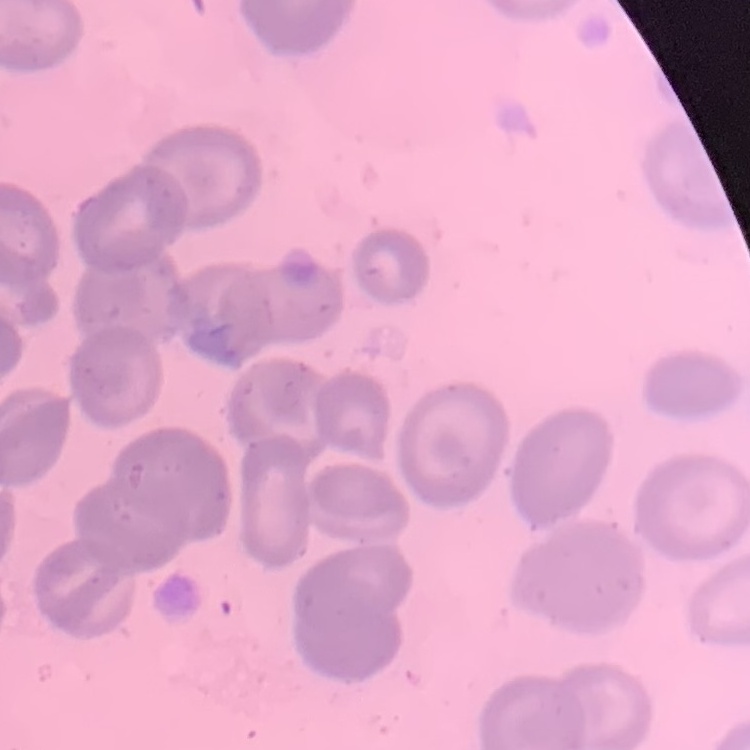
Summary:
  - Erythrocyte morphology: no rouleaux formation
  - Stain: Field's or Giemsa
  - Image type: square crop of a larger photomicrograph
  - Preparation: thin blood smear